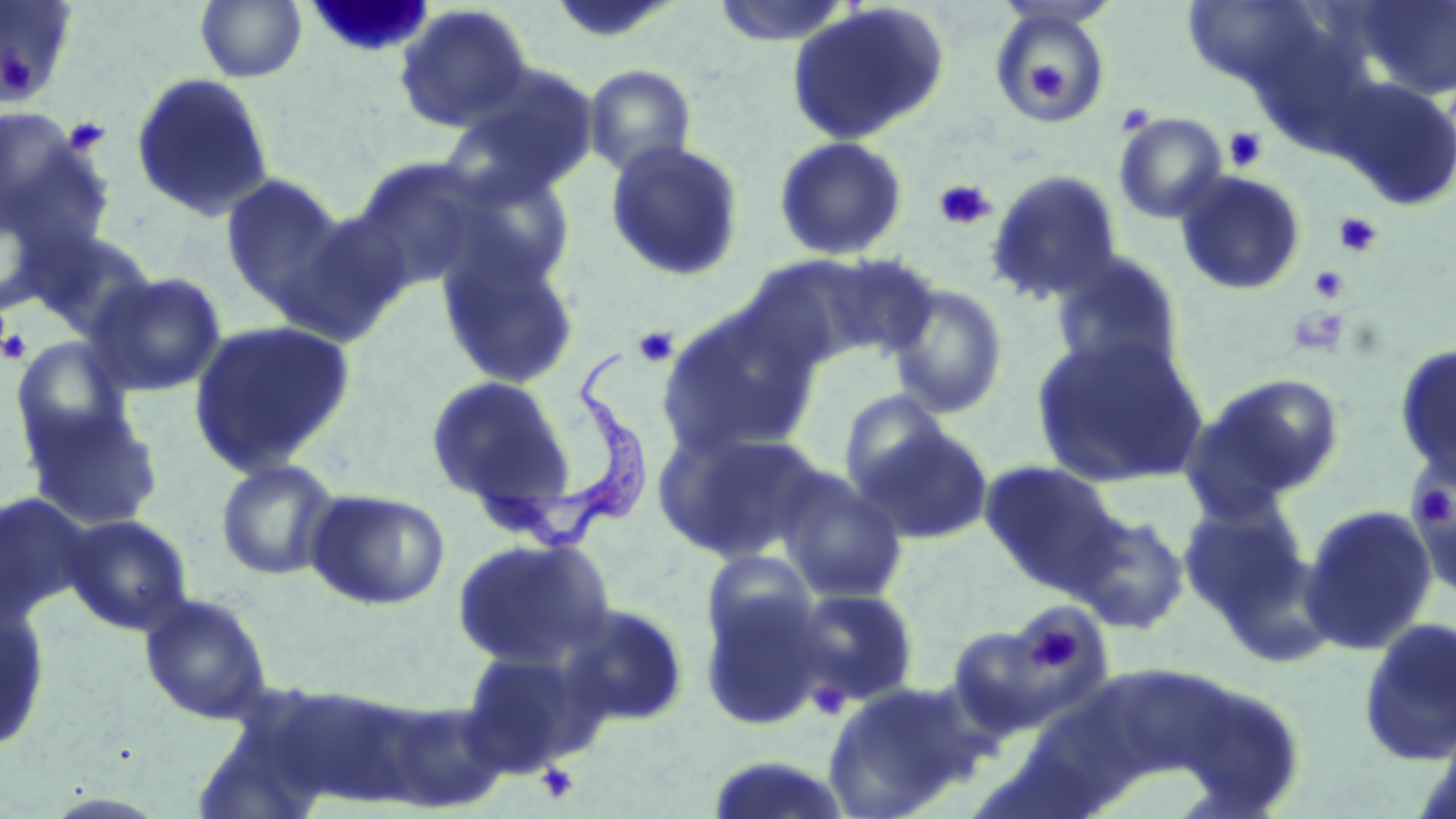
Approximate bounding boxes as [x1, y1, x2, y2] in pixels. Trypanosoma brucei locations: [471, 349, 646, 552]. Uninfected red blood cell locations: [195, 0, 308, 83], [711, 0, 855, 47], [1342, 0, 1456, 102], [0, 1, 78, 108], [1182, 1, 1330, 91], [785, 2, 951, 147], [394, 3, 534, 132], [988, 6, 1115, 125], [583, 63, 697, 179], [129, 72, 276, 223], [1330, 77, 1456, 210], [439, 78, 598, 205], [1113, 112, 1228, 224], [0, 125, 113, 256], [772, 135, 909, 262], [604, 140, 746, 283], [350, 159, 497, 290], [445, 165, 578, 294], [986, 168, 1124, 304], [1174, 170, 1307, 296], [219, 173, 351, 314], [277, 207, 415, 346], [23, 226, 160, 338], [436, 243, 582, 391], [1049, 250, 1185, 376], [815, 253, 941, 363], [84, 270, 228, 397], [885, 281, 1010, 420], [656, 304, 821, 460], [188, 318, 357, 477], [1031, 332, 1208, 489], [10, 336, 136, 451], [1393, 343, 1456, 485], [1193, 372, 1348, 505], [424, 375, 576, 513], [836, 389, 952, 497], [23, 405, 163, 530], [855, 422, 995, 545], [654, 424, 830, 565], [214, 458, 343, 581], [979, 459, 1122, 593], [773, 468, 910, 605], [1409, 479, 1456, 593], [303, 487, 451, 611], [1179, 499, 1313, 630], [1298, 503, 1439, 656], [1071, 511, 1190, 635], [63, 514, 194, 636], [451, 536, 616, 670], [700, 551, 817, 659], [698, 584, 830, 730], [793, 588, 919, 706], [138, 591, 273, 725], [0, 600, 52, 754], [559, 602, 690, 729], [1357, 616, 1456, 766], [946, 624, 1063, 735], [459, 649, 591, 775], [821, 681, 986, 819]. Platelet locations: [3, 55, 31, 97], [1027, 56, 1068, 100], [1114, 102, 1156, 137], [62, 115, 111, 157], [1223, 126, 1268, 172], [934, 179, 998, 231], [1334, 212, 1382, 258], [1308, 265, 1349, 303], [1285, 306, 1351, 356], [632, 325, 680, 368], [0, 327, 31, 365], [1408, 474, 1455, 533], [1023, 620, 1084, 675], [809, 680, 851, 719], [536, 762, 581, 804]. Slide-level diagnosis: Trypanosoma brucei. Image is 1456×819 pixels. Optical microscopy. May-Grünwald-Giemsa-stained preparation. Single field of view. 1000x magnification. Thin blood smear.